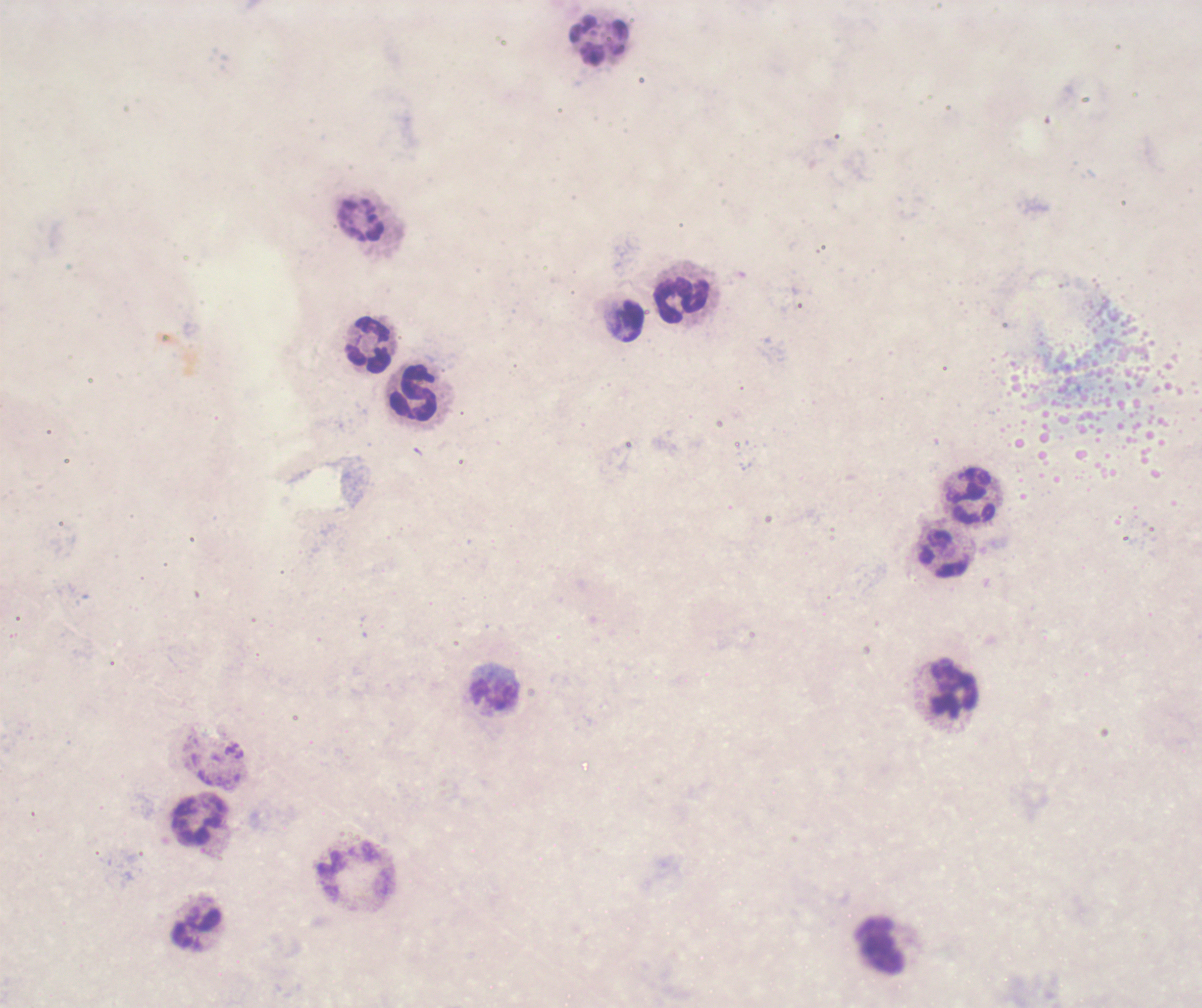

Approximate centers as [x, y] in pixels. Leukocyte locations: [598, 40], [360, 221], [681, 301], [628, 321], [368, 344], [413, 392], [973, 496], [944, 553], [955, 688], [495, 695], [200, 822], [197, 927], [882, 946]. Image is 1202×1008 pixels. Romanowsky stain. Thick smear of blood. Coloration quality: bad. 100x magnification. Background quality: unsatisfactory. Result: no malaria parasites detected. Previously used in an actual diagnosis. One field from this slide.